Give the extent of all uninfected red blood cells.
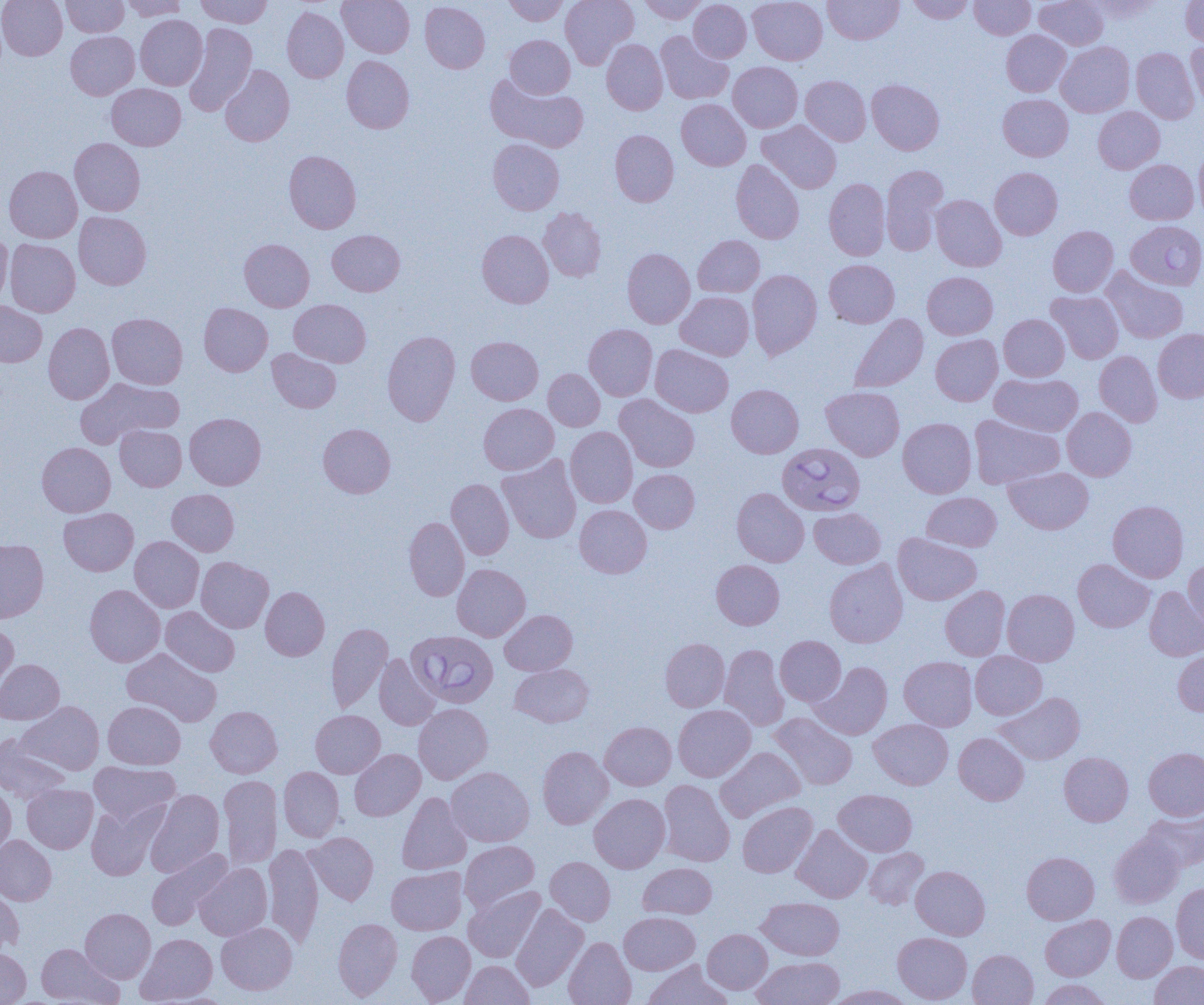
Approximate bounding boxes as (x1, y1, x2, y2) in pixels.
Uninfected red blood cells: (1, 0, 67, 60), (61, 0, 128, 37), (119, 0, 189, 21), (196, 0, 272, 28), (338, 0, 414, 58), (503, 0, 568, 26), (560, 0, 638, 69), (639, 0, 707, 24), (689, 0, 751, 62), (748, 0, 827, 64), (823, 0, 903, 44), (907, 0, 974, 24), (970, 0, 1035, 39), (1035, 0, 1108, 50), (1088, 0, 1163, 20), (1181, 0, 1204, 46), (420, 1, 490, 73), (282, 7, 348, 83), (135, 15, 207, 90), (184, 22, 256, 115), (1001, 30, 1071, 96), (66, 31, 139, 99), (655, 31, 733, 104), (505, 34, 575, 98), (602, 39, 668, 115), (1056, 41, 1135, 117), (1186, 41, 1204, 107), (1131, 48, 1199, 123), (342, 55, 414, 133), (728, 62, 802, 132), (220, 65, 294, 146), (486, 74, 588, 152), (800, 75, 871, 145), (866, 79, 944, 155), (106, 84, 186, 150), (998, 94, 1073, 161), (677, 99, 751, 170), (1093, 106, 1164, 173), (757, 120, 841, 193), (610, 130, 679, 207), (69, 138, 145, 216), (488, 138, 564, 215), (1194, 145, 1204, 221), (284, 150, 361, 233), (731, 159, 804, 244), (1125, 159, 1199, 224), (880, 165, 948, 255), (4, 166, 82, 243), (989, 167, 1062, 240), (824, 178, 890, 260), (931, 195, 1006, 271), (538, 207, 606, 281), (74, 211, 151, 290), (1048, 226, 1118, 297), (327, 229, 405, 296), (477, 230, 554, 308), (0, 231, 13, 307), (693, 235, 764, 297), (5, 239, 80, 317), (239, 239, 314, 311), (622, 248, 695, 328), (824, 259, 899, 327), (1101, 266, 1188, 344), (747, 269, 822, 359), (922, 271, 998, 339), (1046, 291, 1123, 364), (676, 292, 754, 360), (289, 299, 370, 367), (0, 301, 47, 367), (199, 303, 273, 375), (107, 313, 187, 389), (849, 314, 928, 393), (998, 314, 1069, 381), (43, 322, 114, 404), (584, 324, 657, 400), (1153, 328, 1204, 402), (382, 330, 460, 426), (930, 334, 1002, 405), (466, 336, 543, 405), (650, 344, 733, 417), (267, 348, 341, 413), (1094, 351, 1162, 427), (543, 368, 605, 431), (990, 373, 1083, 436), (75, 378, 184, 448), (726, 385, 803, 458), (821, 386, 904, 461), (615, 394, 700, 472), (479, 403, 559, 474), (1062, 407, 1136, 480), (185, 413, 266, 490), (969, 415, 1064, 488), (898, 417, 977, 498), (318, 423, 395, 498), (114, 424, 187, 491), (566, 426, 637, 508), (37, 442, 115, 517), (498, 455, 582, 544), (1005, 467, 1093, 534), (630, 469, 699, 533), (446, 478, 514, 559), (732, 487, 809, 566), (167, 489, 239, 556), (922, 492, 1001, 551), (1108, 500, 1188, 582), (574, 505, 652, 578), (59, 507, 138, 576), (809, 508, 886, 569), (404, 517, 469, 601), (893, 533, 981, 605), (130, 536, 203, 612), (0, 539, 48, 622), (196, 557, 274, 632), (1183, 558, 1204, 635), (824, 559, 908, 648), (1073, 559, 1154, 632), (711, 560, 784, 629), (452, 564, 530, 641), (85, 584, 165, 667), (940, 586, 1010, 660), (1145, 586, 1204, 661), (261, 587, 329, 660), (1002, 588, 1079, 666), (161, 606, 239, 677), (500, 609, 577, 675), (0, 620, 18, 693), (326, 622, 393, 713), (775, 636, 846, 706), (660, 638, 729, 712), (720, 644, 788, 730), (122, 647, 222, 726), (1173, 650, 1204, 715), (970, 651, 1047, 719), (374, 654, 440, 730), (899, 656, 977, 730), (0, 659, 64, 724), (811, 661, 892, 739), (511, 664, 593, 727), (994, 691, 1085, 764), (17, 701, 104, 775), (103, 701, 185, 769), (413, 703, 492, 784), (673, 704, 755, 781), (205, 705, 282, 778), (310, 710, 385, 778), (770, 712, 858, 790), (869, 719, 953, 790), (600, 722, 676, 790), (954, 732, 1029, 805), (0, 735, 71, 803), (537, 746, 613, 828), (715, 746, 805, 821), (1144, 747, 1204, 820), (349, 749, 425, 821), (1059, 752, 1133, 826), (89, 762, 180, 825), (446, 766, 534, 846), (279, 767, 344, 841), (218, 775, 282, 869), (658, 780, 734, 867), (22, 784, 98, 853), (0, 785, 16, 856), (145, 788, 224, 876), (834, 789, 917, 856), (397, 792, 472, 874), (589, 793, 670, 873), (86, 800, 166, 880), (737, 801, 817, 878), (1140, 811, 1204, 872), (792, 824, 872, 903), (305, 832, 378, 904), (1109, 833, 1184, 908), (0, 835, 56, 905), (460, 841, 540, 911), (263, 843, 324, 946), (146, 848, 232, 930), (864, 848, 929, 909), (1022, 852, 1099, 924), (545, 856, 615, 925), (194, 863, 272, 940), (638, 863, 717, 919), (386, 866, 467, 935), (911, 866, 990, 940), (1172, 883, 1204, 962), (0, 885, 24, 955), (464, 886, 544, 962), (757, 897, 844, 960), (511, 903, 588, 991), (80, 908, 155, 983), (619, 911, 699, 975), (1112, 911, 1177, 982), (1040, 915, 1115, 980), (333, 918, 402, 1000), (216, 922, 297, 995), (702, 929, 772, 994), (407, 931, 475, 1004), (893, 932, 972, 1003), (136, 933, 217, 1004), (563, 937, 636, 1005), (36, 943, 121, 1004), (0, 948, 30, 1004), (968, 949, 1038, 1005), (753, 957, 844, 1005), (461, 960, 534, 1005), (642, 960, 732, 1005), (1150, 960, 1204, 1005), (1038, 979, 1110, 1004), (825, 985, 916, 1004).

Summary:
  - Babesia divergens-infected red blood cell locations: (1126, 220, 1204, 291), (777, 443, 865, 516), (407, 630, 498, 708)
  - Slide-level diagnosis: Babesia divergens
  - Magnification: 1000x
  - Preparation: thin blood film
  - Image size: 1204×1005 pixels
  - Field of view: single
  - Modality: optical microscopy